Assess this cell for malaria.
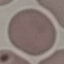
Uninfected.

capture: smartphone through the microscope eyepiece
image_type: automatically extracted cell patch, resized to 64 × 64 pixels
preparation: thin smear
stain: Giemsa